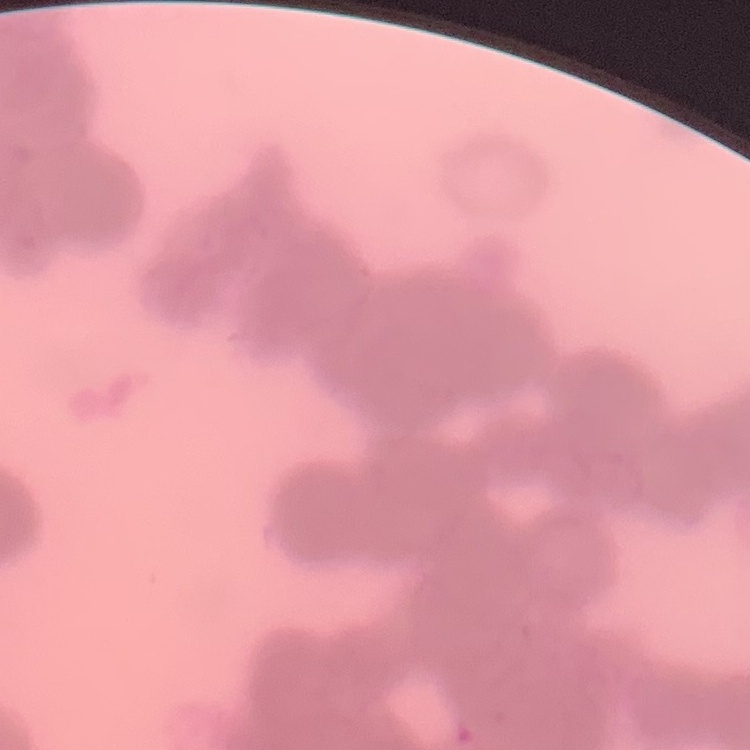 The erythrocytes show rouleaux formation. Field's or Giemsa stain. One tile cut from a larger photomicrograph. Thin blood smear.